Locate every P. falciparum parasite and give its life-cycle stage, and locate every leukocyte and any debris.
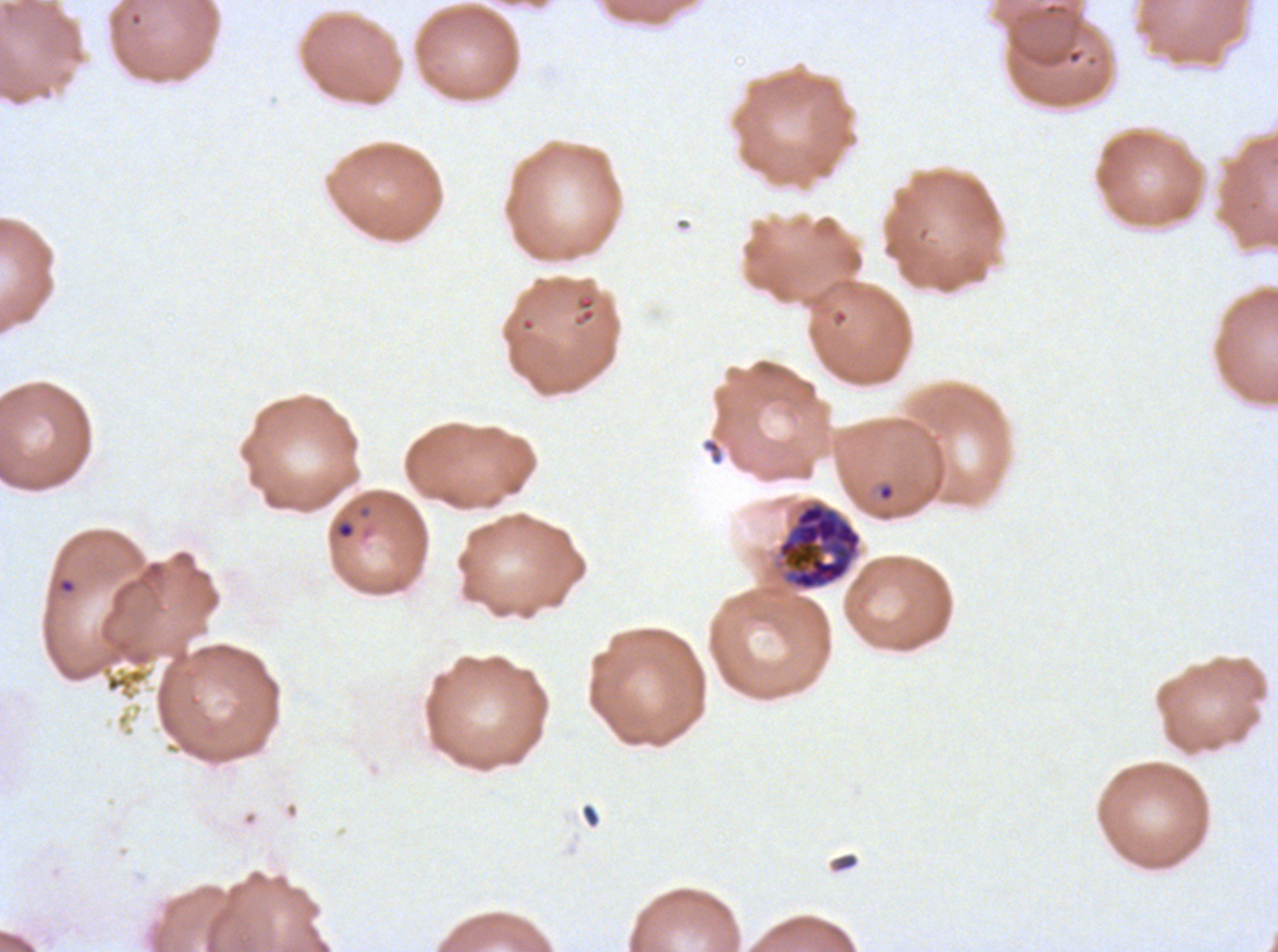

Approximate bounding rectangles given as corner coordinates in pixels from the top-left.
Rings: (x1=337, y1=521, x2=355, y2=539), (x1=57, y1=577, x2=77, y2=595).
Late schizonts: (x1=777, y1=502, x2=862, y2=591).
No late-ring/early-trophozoite forms, mid trophozoites, late trophozoites, early schizonts, segmenters, gametocytes, leukocytes, or debris observed.

stain = Giemsa
preparation = thin blood smear
specimen = P. falciparum from a patient in The Gambia, cultured ex vivo for 24 to 48 hours
image size = 1278×952 pixels
life-cycle stages observed = ring, late schizont
field of view = one sub-image of a larger composite